Assess this cell for malaria.
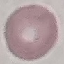

Uninfected.

Summary:
  - Preparation: thin blood film
  - Image type: cell patch, automatically extracted from a larger field of view and resized to 64 × 64 pixels
  - Stain: Giemsa
  - Capture: smartphone camera at the microscope eyepiece